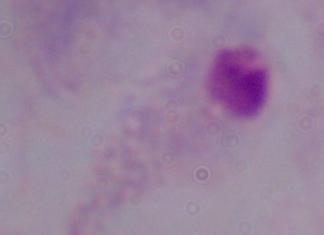

Summary:
  - Magnification: 1000x
  - Modality: photomicrograph
  - Identification: trichomonad